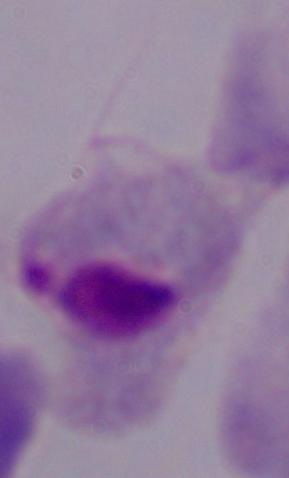
Summary:
  - Modality: micrograph
  - Magnification: 1000x
  - Identification: trichomonad